Classify this cell by malaria status.
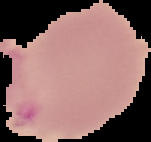

Uninfected.

Summary:
  - Preparation: thin blood smear
  - Image type: segmented cell region with the area outside set to black
  - Image size: 151×142 pixels